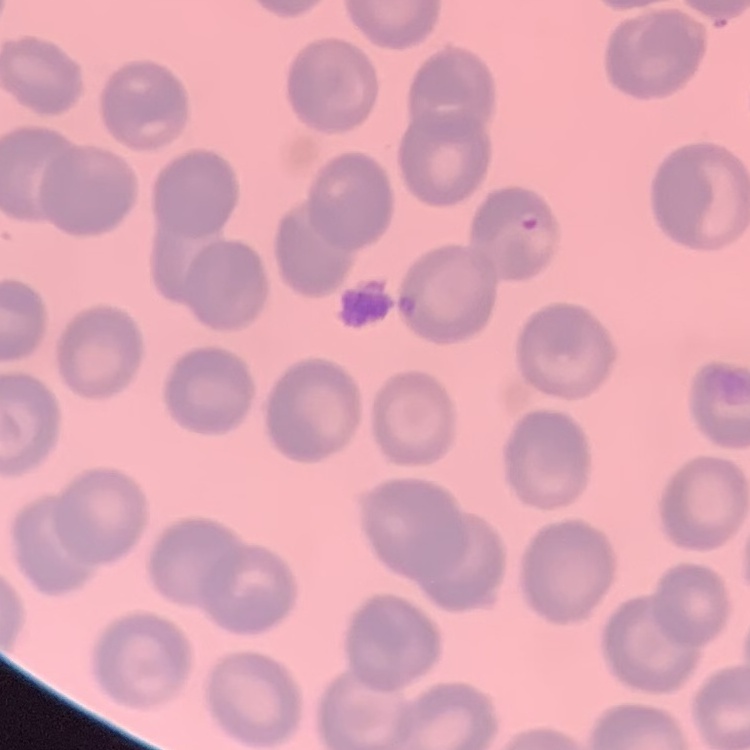

red_blood_cell_morphology: no rouleaux formation
image_type: square crop of a larger photomicrograph
stain: Field's or Giemsa
preparation: thin peripheral smear